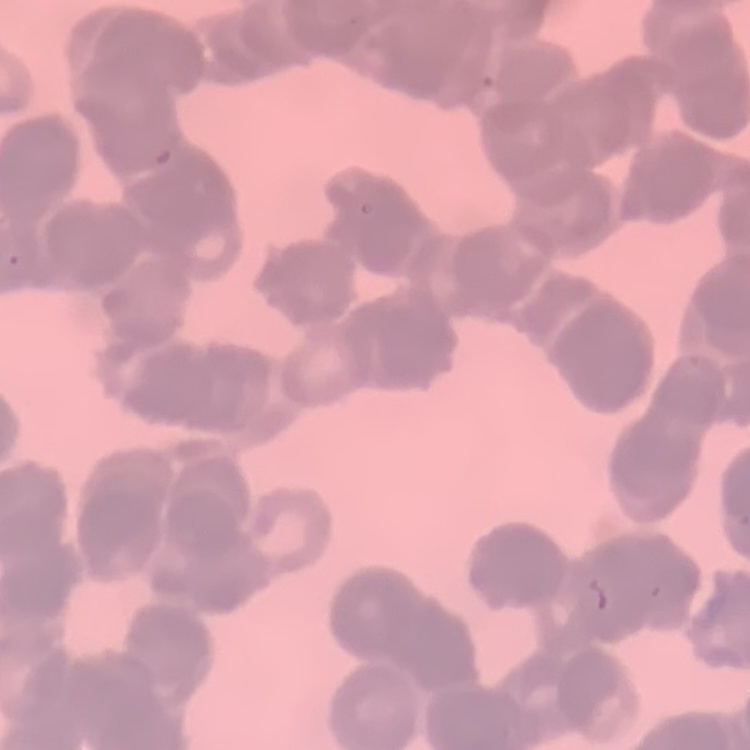

The red blood cells exhibit rouleaux formation. One tile cut from a larger photomicrograph. Field's or Giemsa stain. Thin blood smear.